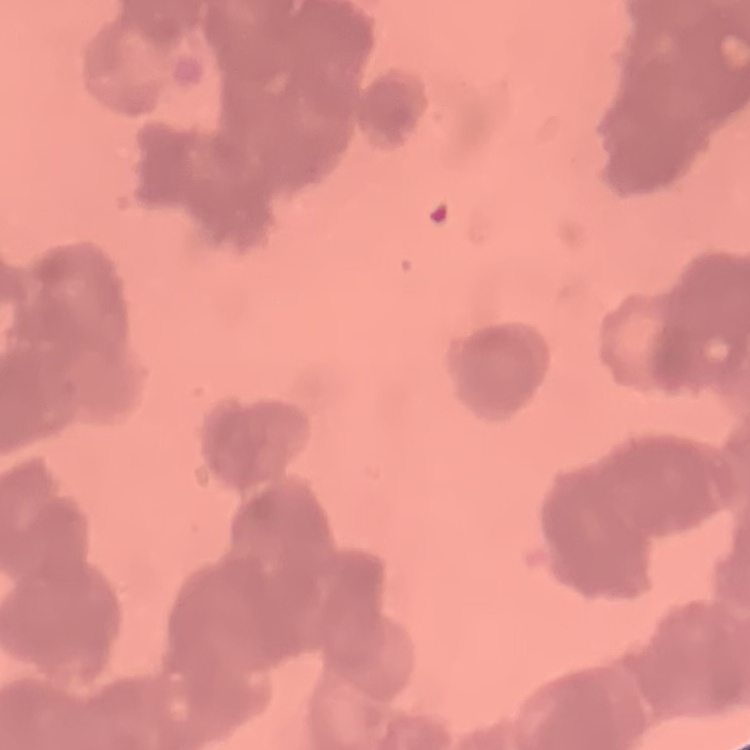
erythrocyte_morphology: rouleaux formation
preparation: thin peripheral smear
image_type: square crop of a larger photomicrograph
stain: Field's or Giemsa